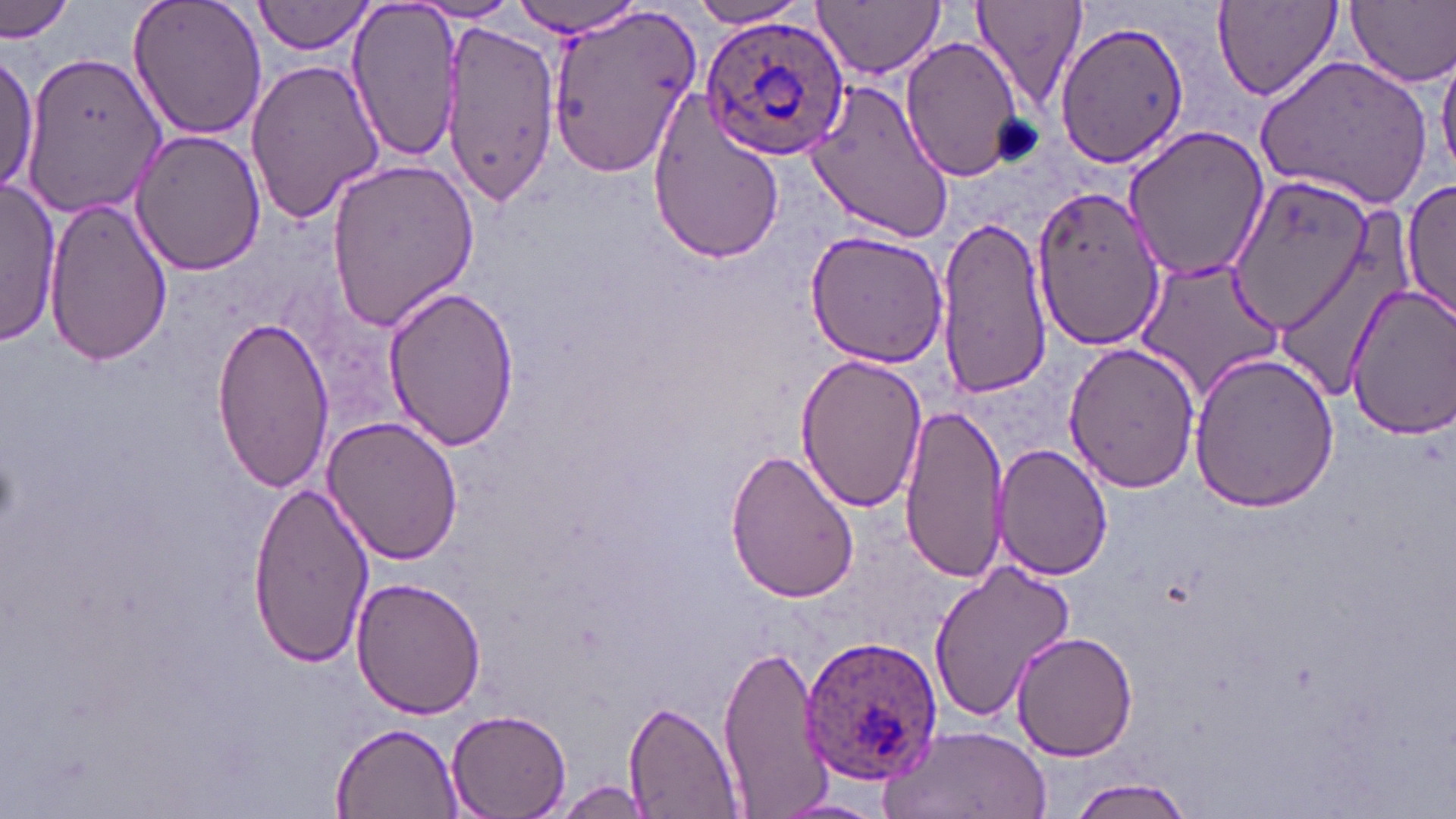

Approximate bounding boxes as (x1,y1)-(x2,y2) corner pairs in pixels. Platelet locations: (990,113)-(1047,168). Uninfected red blood cell locations: (0,0)-(75,44), (125,0)-(269,142), (254,0)-(374,55), (686,0)-(812,29), (814,0)-(946,77), (967,0)-(1088,112), (1212,0)-(1344,104), (1346,0)-(1456,88), (346,1)-(467,162), (409,2)-(524,23), (506,3)-(650,37), (547,5)-(703,178), (440,19)-(559,209), (1055,20)-(1190,169), (899,34)-(1026,183), (1437,43)-(1456,178), (22,48)-(165,214), (0,50)-(43,199), (1256,54)-(1434,209), (244,59)-(386,223), (803,76)-(958,242), (645,92)-(790,261), (1121,123)-(1270,285), (129,128)-(265,275), (324,156)-(479,334), (1399,177)-(1455,322), (0,179)-(61,345), (1030,183)-(1167,349), (45,195)-(173,366), (932,214)-(1055,403), (1271,224)-(1414,405), (804,228)-(952,367), (1135,256)-(1286,397), (380,284)-(520,451), (1343,284)-(1456,440), (208,314)-(334,492), (1062,340)-(1201,493), (795,354)-(927,514), (1188,354)-(1342,512), (900,403)-(1011,581), (320,414)-(463,566), (993,443)-(1111,580), (723,445)-(860,604), (245,479)-(374,665), (928,560)-(1076,722), (352,575)-(487,720), (1011,630)-(1139,762), (716,643)-(833,814), (625,702)-(741,818), (445,709)-(570,819), (327,718)-(462,817), (877,723)-(1051,819), (1068,776)-(1198,818), (548,780)-(661,817), (767,797)-(890,818). Plasmodium ovale-infected red blood cell locations: (700,12)-(852,161), (796,632)-(944,785). Slide-level diagnosis: Plasmodium ovale. Image is 1456×819 pixels. Thin blood smear. Single field of view. May-Grünwald-Giemsa stain. Light microscopy. Captured at 1000x magnification.